Report the malaria status of this cell.
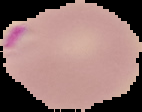

It is parasitized.

preparation = thin blood film
image type = cell region segmented out of the field of view; surrounding area masked to black
image size = 142×112 pixels